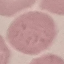

Summary:
  - Malaria status: uninfected
  - Preparation: thin blood film
  - Image type: automatically extracted cell patch, resized to 64 × 64 pixels
  - Capture: smartphone through the microscope eyepiece
  - Stain: Giemsa